Locate every leukocyte (white blood cell).
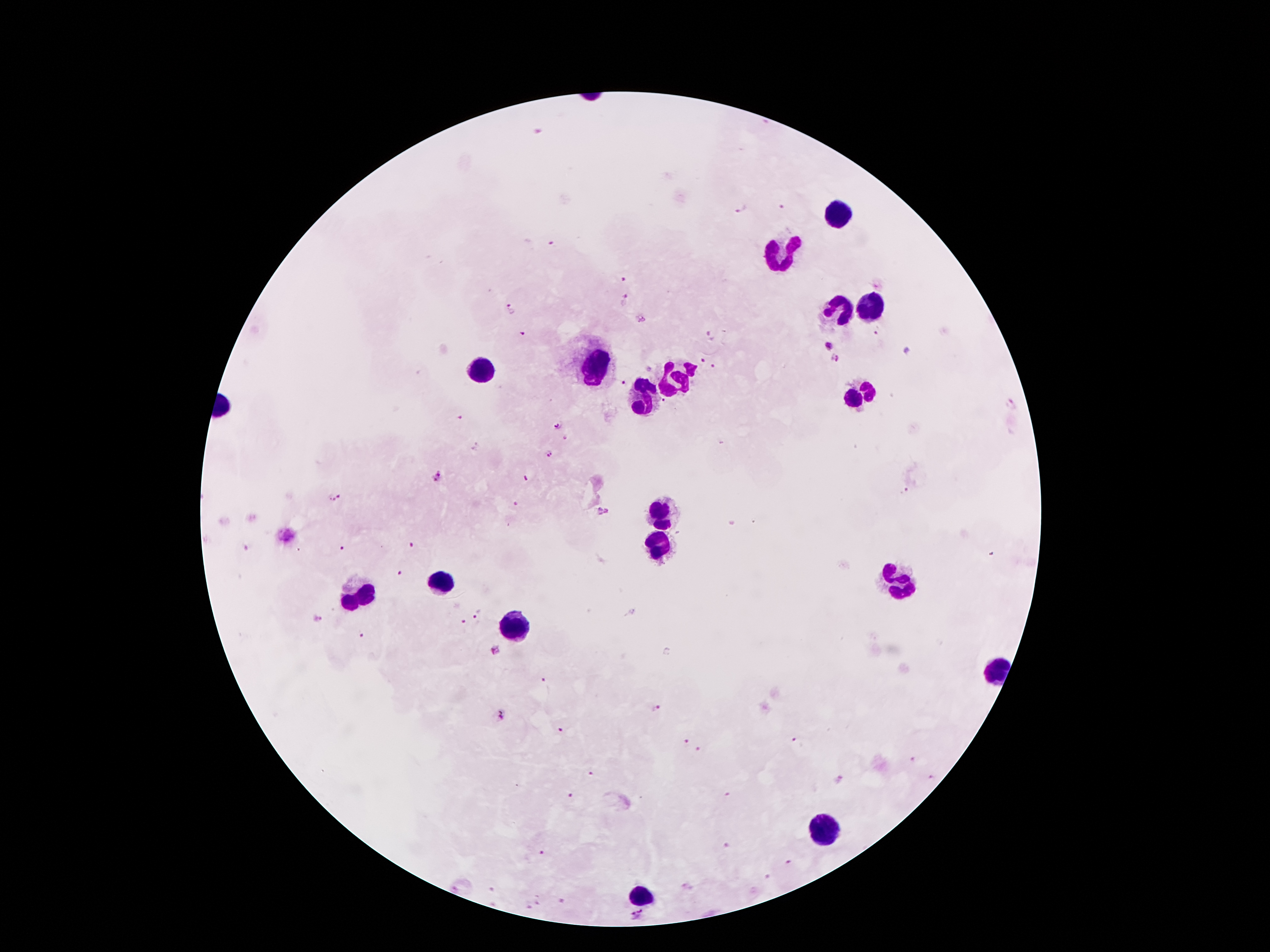

Approximate centers as {x, y} in pixels.
Leukocytes: {842, 213}, {778, 254}, {837, 309}, {867, 309}, {597, 366}, {479, 372}, {674, 375}, {861, 394}, {645, 397}, {665, 511}, {660, 541}, {901, 577}, {436, 584}, {358, 597}, {513, 628}, {996, 674}, {819, 831}, {644, 892}.

Plasmodium parasite locations: {538, 131}, {742, 208}, {780, 208}, {553, 244}, {624, 276}, {624, 300}, {512, 309}, {641, 318}, {524, 333}, {880, 333}, {714, 334}, {829, 347}, {834, 359}, {702, 362}, {715, 367}, {623, 383}, {1010, 405}, {461, 418}, {557, 425}, {564, 438}, {548, 455}, {440, 478}, {527, 478}, {907, 492}, {334, 499}, {519, 503}, {604, 512}, {413, 545}, {245, 548}, {343, 549}, {401, 571}, {477, 615}, {317, 617}, {463, 624}, {362, 637}, {497, 649}, {543, 680}, {655, 709}, {500, 716}, {560, 731}, {686, 740}, {796, 740}, {699, 753}, {912, 758}, {590, 773}, {931, 778}, {838, 780}, {570, 794}, {729, 795}, {726, 846}, {543, 853}, {787, 863}, {767, 876}, {688, 887}, {455, 889}, {561, 900}, {540, 903}, {529, 907}, {638, 917}. Smartphone photograph taken through the microscope eyepiece. One field from this slide. 100x magnification. Patient malaria status: infected with Plasmodium falciparum. Thick blood smear. Giemsa stain. Image is 1270×952 pixels.